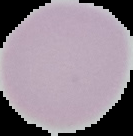

Summary:
  - Image type: segmented cell region with the area outside set to black
  - Preparation: thin blood film
  - Image size: 133×136 pixels
  - Malaria status: uninfected